Give the extent of all Plasmodium ovale-infected red blood cells.
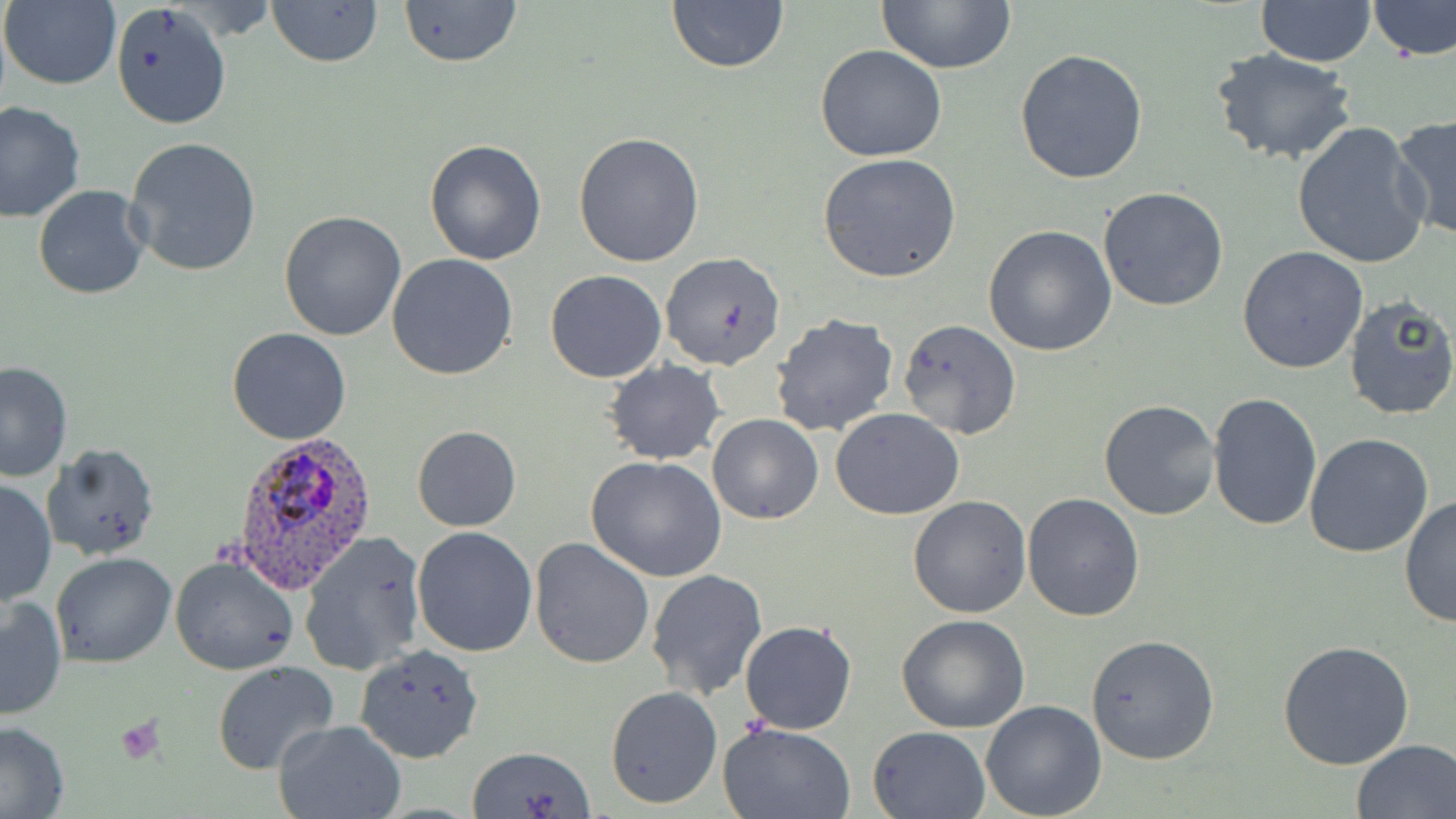

Approximate bounding boxes as named x1/y1/x2/y2 corners in pixels.
Plasmodium ovale-infected red blood cells: (x1=228, y1=428, x2=378, y2=592).

slide-level diagnosis = Plasmodium ovale
uninfected red blood cell locations = approximate bounding boxes as named x1/y1/x2/y2 corners in pixels: (x1=265, y1=0, x2=384, y2=68), (x1=398, y1=0, x2=524, y2=69), (x1=876, y1=0, x2=1017, y2=72), (x1=2, y1=1, x2=121, y2=91), (x1=110, y1=1, x2=231, y2=129), (x1=666, y1=1, x2=788, y2=72), (x1=1369, y1=1, x2=1456, y2=61), (x1=1256, y1=2, x2=1376, y2=67), (x1=814, y1=46, x2=948, y2=163), (x1=1014, y1=47, x2=1148, y2=184), (x1=1211, y1=50, x2=1358, y2=166), (x1=0, y1=101, x2=86, y2=222), (x1=1390, y1=116, x2=1456, y2=243), (x1=1291, y1=121, x2=1430, y2=270), (x1=574, y1=131, x2=706, y2=268), (x1=124, y1=137, x2=263, y2=277), (x1=424, y1=138, x2=547, y2=266), (x1=818, y1=153, x2=962, y2=283), (x1=32, y1=183, x2=151, y2=300), (x1=1098, y1=186, x2=1230, y2=312), (x1=279, y1=210, x2=406, y2=342), (x1=983, y1=226, x2=1118, y2=357), (x1=1237, y1=246, x2=1370, y2=374), (x1=660, y1=251, x2=788, y2=372), (x1=387, y1=254, x2=518, y2=379), (x1=544, y1=269, x2=668, y2=383), (x1=1343, y1=295, x2=1456, y2=421), (x1=769, y1=314, x2=899, y2=438), (x1=897, y1=320, x2=1021, y2=439), (x1=225, y1=328, x2=351, y2=445), (x1=0, y1=360, x2=73, y2=483), (x1=603, y1=361, x2=726, y2=464), (x1=1208, y1=392, x2=1323, y2=530), (x1=1099, y1=398, x2=1221, y2=520), (x1=830, y1=409, x2=965, y2=521), (x1=707, y1=413, x2=824, y2=524), (x1=412, y1=425, x2=522, y2=532), (x1=1304, y1=434, x2=1435, y2=559), (x1=40, y1=443, x2=160, y2=562), (x1=586, y1=455, x2=727, y2=582), (x1=0, y1=477, x2=56, y2=608), (x1=1023, y1=493, x2=1145, y2=623), (x1=907, y1=495, x2=1032, y2=618), (x1=1400, y1=496, x2=1455, y2=628), (x1=411, y1=526, x2=537, y2=657), (x1=298, y1=529, x2=428, y2=677), (x1=529, y1=537, x2=655, y2=668), (x1=51, y1=552, x2=177, y2=668), (x1=170, y1=554, x2=299, y2=676), (x1=645, y1=569, x2=767, y2=701), (x1=0, y1=593, x2=68, y2=720), (x1=897, y1=613, x2=1029, y2=733), (x1=738, y1=620, x2=857, y2=736), (x1=1085, y1=633, x2=1220, y2=764), (x1=1277, y1=638, x2=1416, y2=772), (x1=355, y1=644, x2=486, y2=763), (x1=212, y1=661, x2=339, y2=775), (x1=605, y1=685, x2=722, y2=807), (x1=980, y1=700, x2=1107, y2=819), (x1=273, y1=718, x2=407, y2=819), (x1=0, y1=722, x2=71, y2=819), (x1=719, y1=722, x2=858, y2=819), (x1=868, y1=726, x2=990, y2=819), (x1=1350, y1=738, x2=1456, y2=819), (x1=469, y1=745, x2=594, y2=819)
modality = optical microscopy
platelet locations = approximate bounding boxes as named x1/y1/x2/y2 corners in pixels: (x1=113, y1=714, x2=166, y2=765)
field of view = one of a larger specimen
preparation = thin blood film
stain = May-Grünwald-Giemsa
image size = 1456×819 pixels
magnification = 1000x